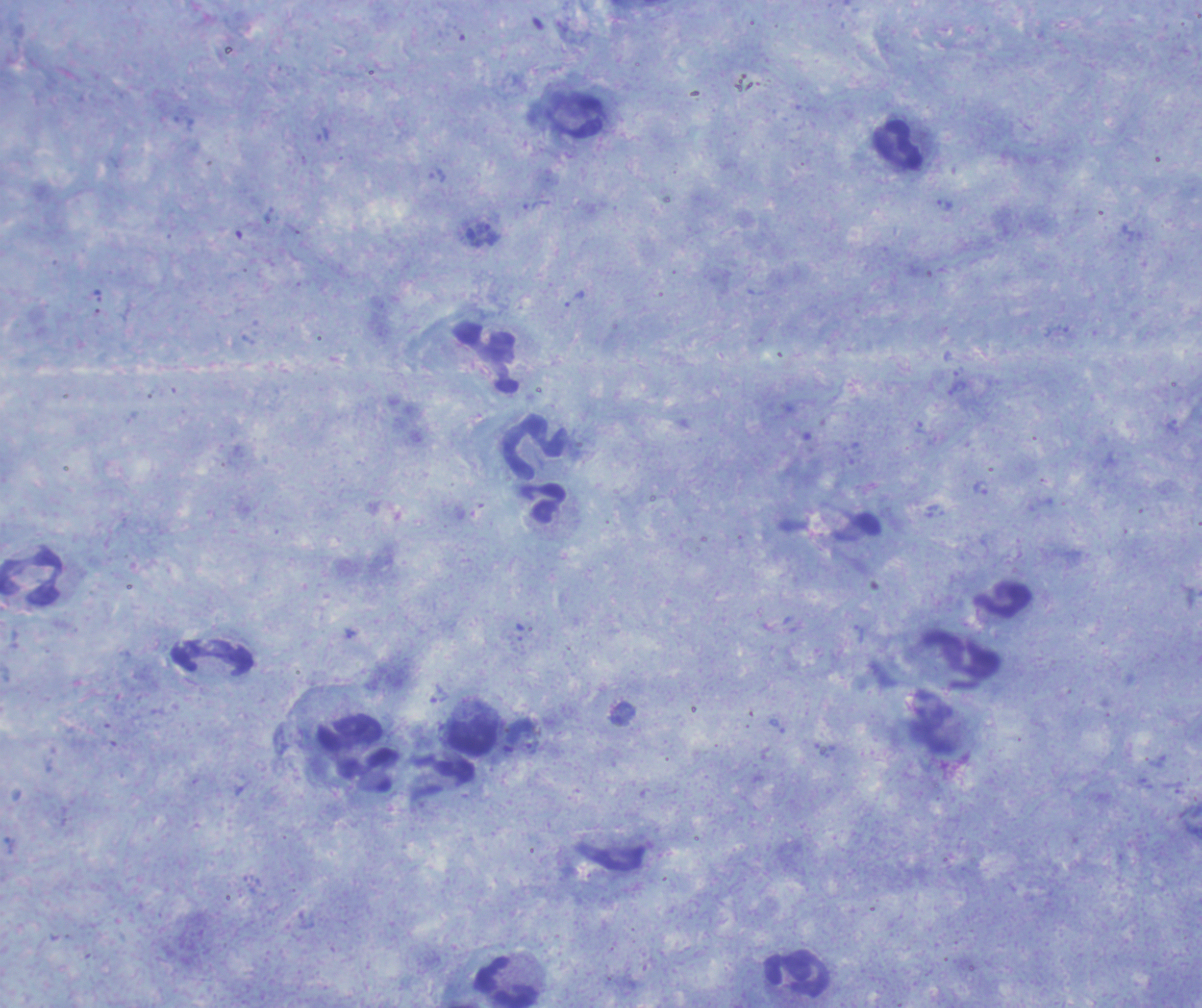

Approximate centers as (x, y) in pixels.
Summary:
  - Leukocyte locations: (898, 145), (486, 357), (533, 447), (543, 503), (30, 578), (1003, 601), (965, 659), (471, 738), (357, 747), (796, 973), (507, 983)
  - Trophozoite locations: (945, 205), (491, 235), (575, 298), (980, 488), (520, 632), (438, 693), (623, 714), (530, 746)
  - Context: previously used in an actual diagnosis
  - Image size: 1202×1008 pixels
  - Magnification: 100x
  - Background quality: good
  - Preparation: thick blood smear
  - Result: positive for Plasmodium parasites
  - Field of view: single
  - Coloration quality: good
  - Stain: Romanowsky